Locate every blood parasite and identify its species.
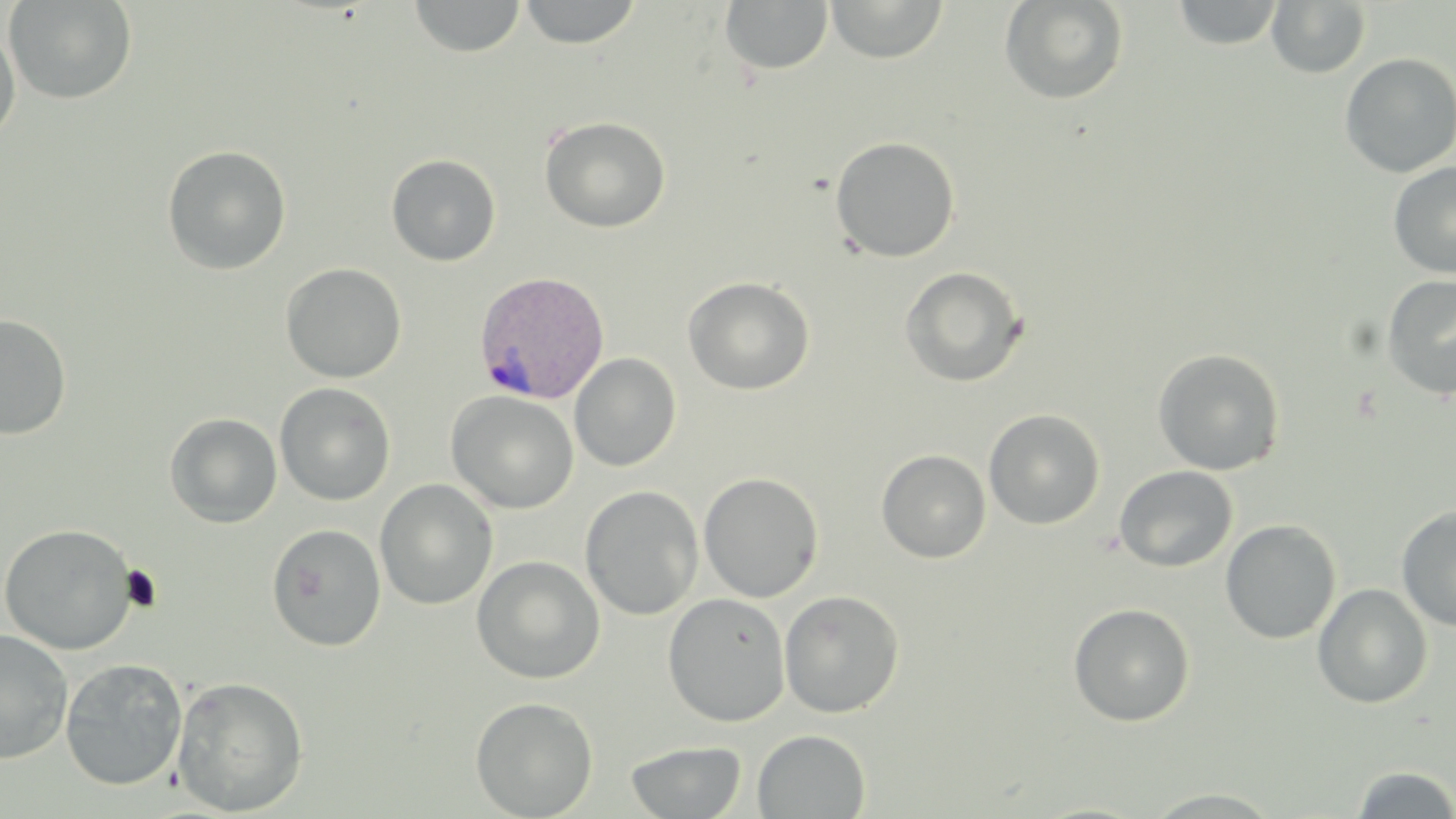

Approximate bounding boxes as (x1, y1, x2, y2) in pixels.
Plasmodium vivax-infected red blood cells: (473, 270, 611, 405).
No Plasmodium falciparum, Plasmodium ovale, Plasmodium malariae, Babesia divergens, or Trypanosoma brucei observed.

Platelet locations: (119, 566, 162, 612). Uninfected red blood cell locations: (4, 0, 137, 105), (408, 0, 526, 58), (517, 0, 642, 48), (827, 0, 948, 63), (999, 0, 1129, 105), (720, 1, 835, 77), (1170, 1, 1286, 49), (1267, 1, 1371, 78), (0, 24, 21, 144), (1339, 52, 1456, 178), (539, 116, 671, 232), (829, 135, 961, 262), (162, 145, 291, 275), (386, 153, 501, 266), (1388, 161, 1456, 279), (280, 262, 407, 383), (898, 266, 1028, 387), (1381, 274, 1456, 400), (682, 276, 815, 395), (0, 315, 72, 439), (1152, 348, 1286, 475), (569, 353, 681, 472), (274, 382, 396, 505), (445, 390, 578, 514), (983, 408, 1105, 530), (165, 412, 283, 528), (876, 449, 991, 563), (1114, 465, 1238, 572), (698, 472, 824, 603), (374, 478, 498, 610), (580, 485, 704, 620), (1396, 505, 1456, 633), (1220, 519, 1341, 644), (0, 523, 137, 654), (267, 523, 386, 651), (471, 555, 605, 684), (1312, 583, 1432, 709), (779, 589, 905, 718), (663, 592, 791, 727), (1068, 603, 1195, 727), (0, 629, 73, 765), (60, 657, 188, 790), (171, 675, 309, 816), (470, 696, 598, 818), (753, 730, 871, 818), (626, 740, 746, 818), (1348, 765, 1456, 817), (1142, 788, 1283, 817). Slide-level diagnosis: Plasmodium vivax. Optical microscopy. Captured at 1000x magnification. May-Grünwald-Giemsa stain. Image is 1456×819 pixels. Thin blood smear. Single field of view.